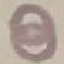

Malaria status: uninfected. Photographed with a smartphone camera at the microscope eyepiece. Automatically extracted cell patch, resized to 64 × 64 pixels. Giemsa-stained preparation. Thin smear of blood.